Point out each leukocyte.
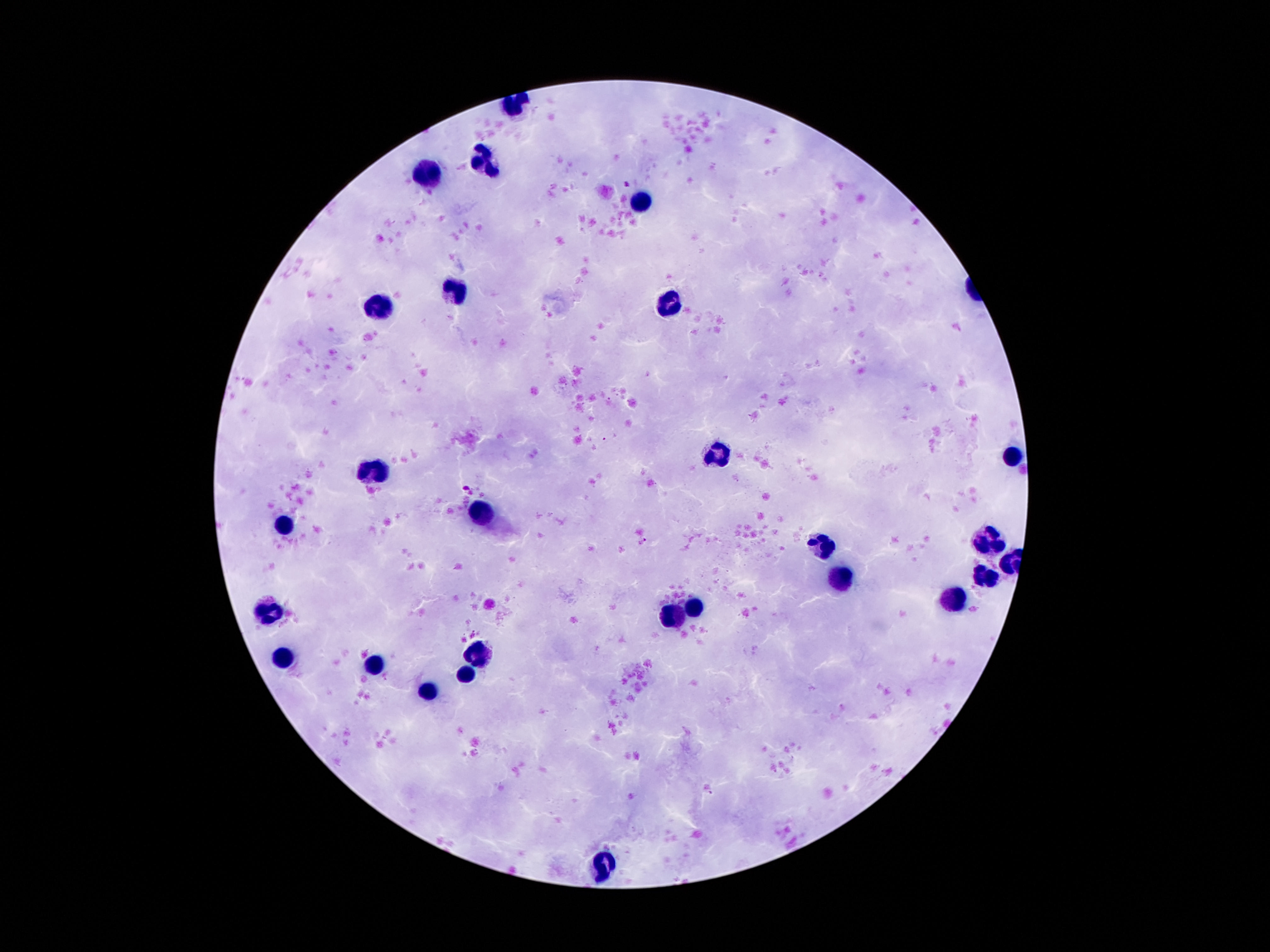
Approximate object centers, in pixels from the top-left corner.
Leukocytes: (x=485, y=157), (x=431, y=174), (x=643, y=202), (x=457, y=288), (x=670, y=304), (x=378, y=308), (x=716, y=453), (x=1013, y=455), (x=376, y=472), (x=479, y=512), (x=283, y=527), (x=989, y=542), (x=823, y=545), (x=985, y=573), (x=839, y=579), (x=955, y=598), (x=696, y=610), (x=270, y=611), (x=677, y=614), (x=477, y=651), (x=285, y=657), (x=375, y=659), (x=466, y=674), (x=427, y=691), (x=600, y=866).

preparation = thick blood film
patient malaria status = not infected
stain = Giemsa
magnification = 100x
field of view = single
capture = smartphone camera through the microscope eyepiece
image size = 1270×952 pixels